Describe the morphology of the erythrocytes.
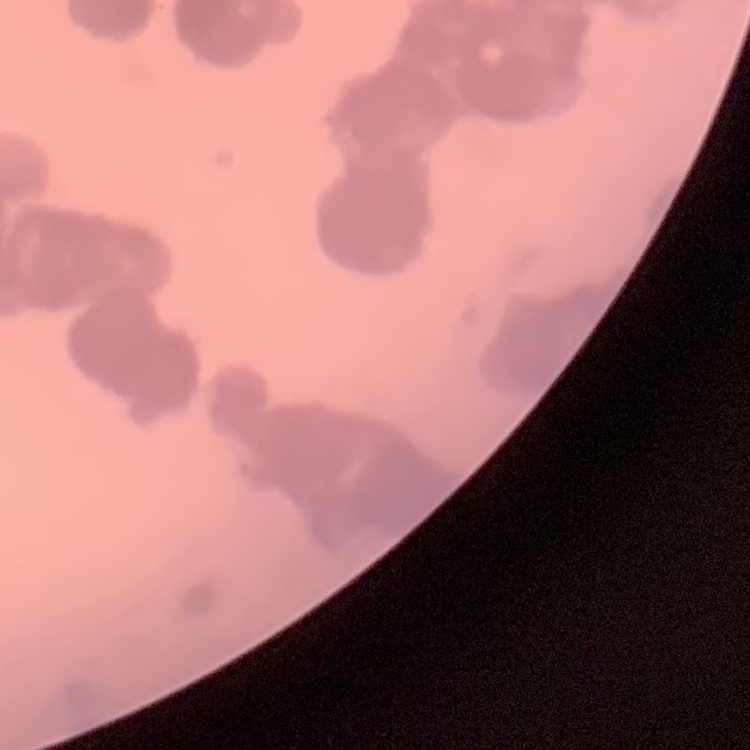
Rouleaux formation.

stain = Field's or Giemsa
image type = square crop of a larger photomicrograph
preparation = thin blood smear